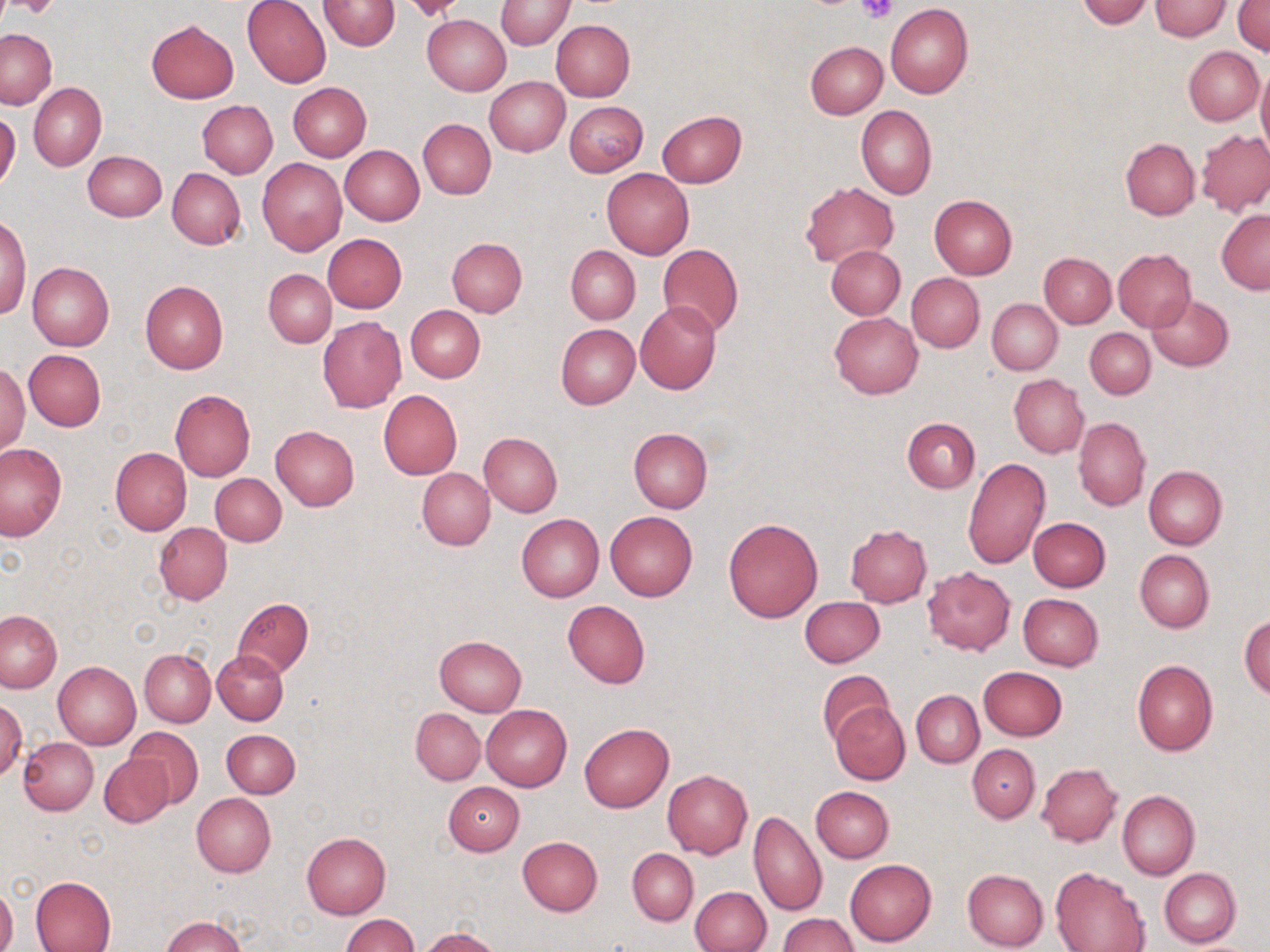
Summary:
  - Coordinate format: approximate bounding boxes as (x1,y1)-(x2,y2) corner pairs in pixels
  - Platelet locations: (7,0)-(62,20), (856,0)-(898,24)
  - Uninfected red blood cell locations: (4,0)-(60,18), (242,0)-(332,87), (320,0)-(399,51), (1077,0)-(1153,27), (1149,0)-(1230,40), (496,1)-(573,49), (1233,2)-(1270,54), (885,4)-(973,98), (422,14)-(511,95), (146,19)-(239,102), (550,19)-(635,101), (0,28)-(56,109), (804,42)-(887,119), (1184,46)-(1264,124), (1257,63)-(1270,159), (486,77)-(569,155), (29,82)-(106,170), (287,82)-(371,161), (197,101)-(278,178), (565,101)-(647,177), (857,105)-(937,199), (657,110)-(746,188), (0,111)-(20,189), (418,118)-(495,199), (1196,129)-(1270,215), (1120,138)-(1199,219), (340,145)-(424,225), (83,151)-(166,221), (257,158)-(347,255), (167,168)-(245,250), (602,169)-(694,259), (801,182)-(900,266), (929,193)-(1017,278), (1217,210)-(1270,293), (0,215)-(31,317), (322,234)-(407,313), (447,237)-(527,316), (659,243)-(743,337), (826,245)-(905,319), (565,246)-(640,323), (1113,249)-(1195,329), (1040,253)-(1116,328), (26,262)-(114,350), (264,269)-(335,347), (907,273)-(984,351), (140,280)-(229,374), (1147,293)-(1234,371), (988,299)-(1062,374), (635,302)-(721,394), (405,305)-(485,382), (829,311)-(922,399), (317,316)-(407,413), (556,324)-(638,408), (1085,327)-(1155,399), (24,350)-(106,431), (0,362)-(29,456), (1009,374)-(1088,458), (170,389)-(255,481), (378,389)-(462,478), (1074,416)-(1150,511), (902,417)-(980,493), (270,426)-(359,511), (628,429)-(713,512), (479,432)-(562,516), (0,443)-(66,540), (110,447)-(191,536), (963,458)-(1050,569), (1144,465)-(1227,549), (417,467)-(494,550), (210,474)-(286,546), (605,511)-(697,600), (516,513)-(603,601), (1029,517)-(1110,591), (723,518)-(822,621), (154,523)-(232,604), (845,525)-(933,606), (1135,549)-(1214,633), (923,566)-(1015,655), (1018,593)-(1103,670), (232,597)-(313,678), (800,597)-(885,667), (563,600)-(650,689), (0,611)-(61,692), (1240,616)-(1269,699), (434,635)-(526,715), (140,649)-(216,726), (213,651)-(287,724), (54,660)-(140,749), (1132,660)-(1218,756), (978,666)-(1067,741), (817,670)-(894,746), (911,689)-(984,767), (0,699)-(25,782), (829,701)-(910,785), (481,704)-(571,790), (411,708)-(484,785), (579,722)-(674,811), (124,726)-(204,807), (221,729)-(300,798), (19,736)-(98,815), (966,744)-(1039,822), (100,753)-(174,828), (1036,763)-(1122,845), (662,770)-(753,858), (442,782)-(523,855), (811,786)-(894,862), (1117,790)-(1199,880), (191,793)-(276,877), (749,810)-(826,916), (301,832)-(390,918), (517,836)-(602,916), (627,847)-(697,924), (846,858)-(937,945), (1050,866)-(1150,952), (1159,867)-(1241,948), (961,868)-(1048,951), (30,875)-(116,952), (0,884)-(17,952), (691,886)-(771,952), (778,913)-(859,952), (162,914)-(245,952), (342,915)-(419,952), (418,927)-(501,951)
  - Slide-level diagnosis: negative for blood parasites
  - Image size: 1270×952 pixels
  - Magnification: 1000x
  - Field of view: one of a larger specimen
  - Modality: light microscopy
  - Preparation: thin blood smear
  - Stain: May-Grünwald-Giemsa